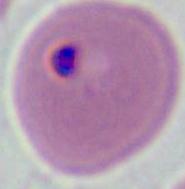

Photomicrograph. A Plasmodium parasite is seen. Captured at either 400x or 1000x magnification.